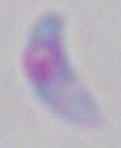
Summary:
  - Magnification: 1000x
  - Identification: Toxoplasma gondii
  - Modality: photomicrograph